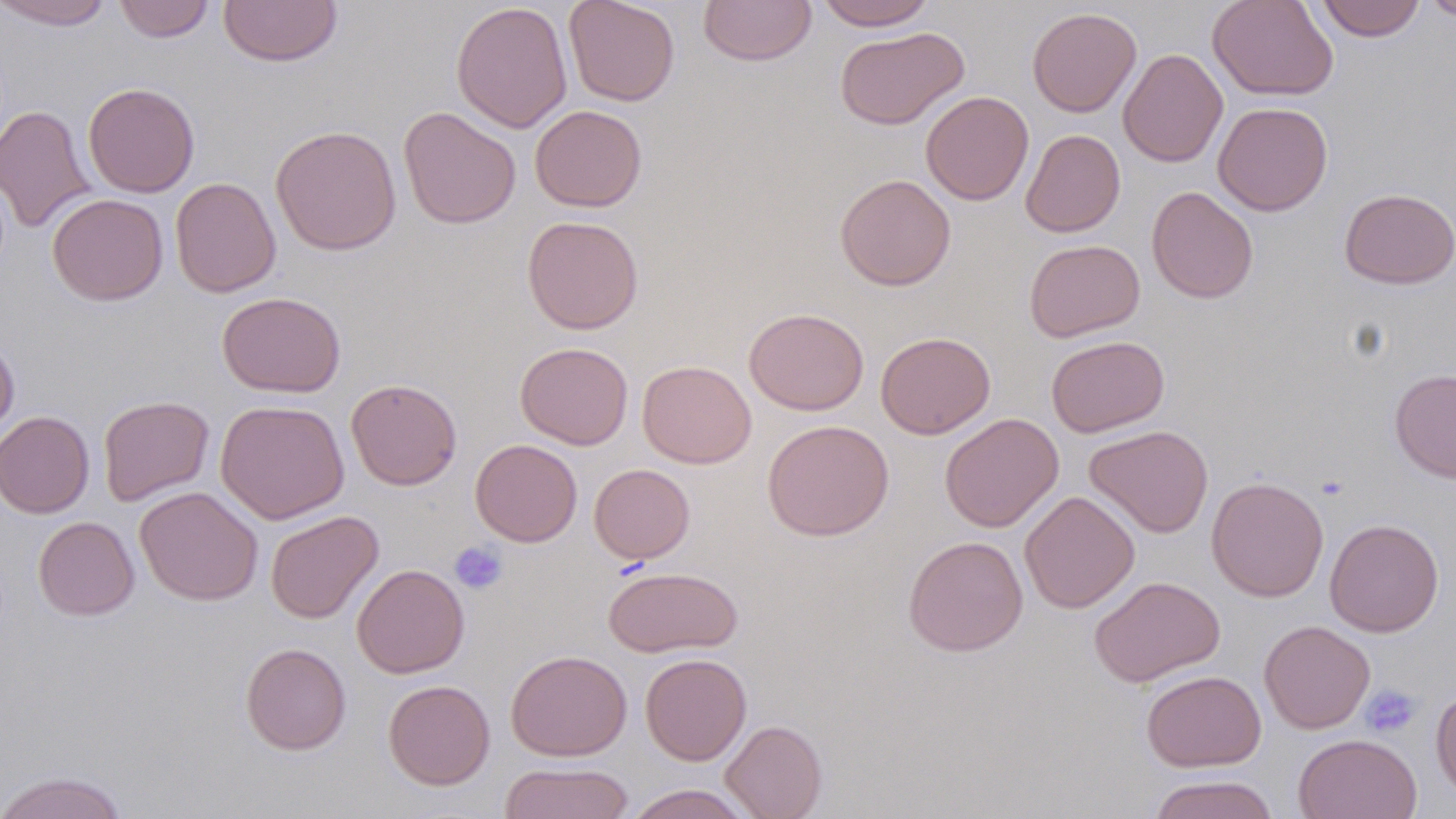 Approximate bounding boxes as [x1, y1, x2, y2] in pixels. Platelet locations: [449, 541, 508, 595], [1359, 684, 1422, 739]. Uninfected red blood cell locations: [1, 0, 115, 29], [113, 0, 215, 43], [218, 0, 343, 67], [564, 0, 681, 106], [699, 0, 817, 66], [814, 0, 936, 30], [1207, 0, 1339, 101], [1420, 0, 1456, 22], [451, 1, 573, 133], [1316, 1, 1426, 41], [1027, 7, 1142, 117], [834, 26, 969, 130], [1118, 48, 1228, 167], [83, 82, 200, 197], [920, 90, 1033, 205], [1213, 101, 1333, 216], [0, 104, 96, 234], [529, 105, 647, 212], [398, 106, 522, 230], [270, 124, 401, 256], [1020, 129, 1125, 237], [835, 173, 956, 291], [170, 177, 282, 298], [1146, 186, 1259, 303], [1338, 188, 1456, 289], [47, 193, 168, 306], [521, 215, 644, 334], [1023, 239, 1145, 342], [216, 291, 346, 397], [744, 307, 869, 415], [876, 331, 996, 439], [1046, 335, 1169, 437], [0, 336, 19, 443], [515, 342, 634, 450], [637, 360, 756, 469], [1389, 368, 1456, 482], [346, 378, 462, 490], [97, 395, 215, 506], [215, 398, 349, 524], [0, 411, 94, 518], [939, 413, 1064, 532], [762, 419, 894, 541], [1085, 424, 1214, 538], [469, 439, 582, 546], [589, 463, 695, 564], [1206, 476, 1329, 602], [134, 486, 264, 606], [1020, 491, 1140, 614], [265, 510, 383, 624], [33, 516, 139, 620], [1324, 518, 1443, 637], [903, 535, 1028, 656], [351, 563, 470, 678], [603, 566, 743, 657], [1088, 575, 1226, 688], [1259, 620, 1375, 734], [240, 642, 351, 755], [505, 649, 632, 762], [640, 652, 752, 765], [1141, 670, 1266, 772], [383, 679, 495, 789], [1430, 687, 1456, 801], [720, 719, 828, 819], [1293, 733, 1422, 819], [498, 761, 634, 819], [0, 770, 129, 819], [1148, 774, 1280, 819], [623, 784, 756, 818]. Slide-level diagnosis: no evidence of blood parasites. May-Grünwald-Giemsa-stained preparation. One field of a larger specimen. Thin blood smear. Image is 1456×819 pixels. 1000x magnification. Optical microscopy.